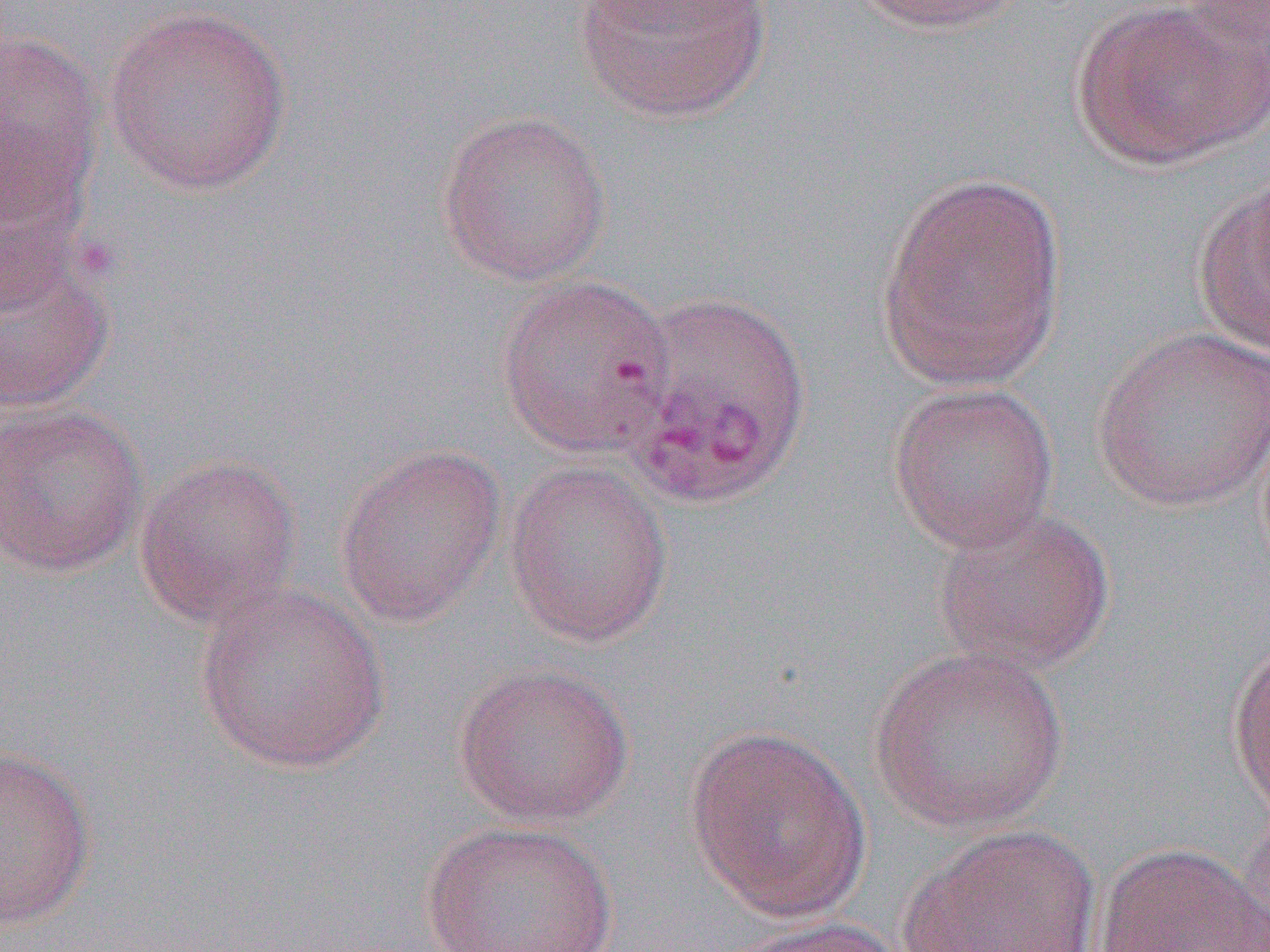
slide-level diagnosis = Plasmodium vivax
magnification = 1000x
field of view = single
modality = light microscopy
preparation = thin blood smear
image size = 1270×952 pixels
uninfected red blood cell locations (subset) = approximate bounding boxes as [x1, y1, x2, y2] in pixels: [581, 0, 771, 33], [845, 0, 1031, 35], [1070, 0, 1264, 169], [572, 1, 773, 124], [102, 6, 293, 196], [0, 30, 104, 215], [435, 109, 613, 286], [875, 168, 1069, 391], [1191, 170, 1270, 360], [0, 241, 116, 413], [495, 274, 676, 457], [1092, 326, 1270, 512], [887, 382, 1060, 553], [0, 400, 149, 579], [333, 443, 507, 627], [133, 453, 303, 629], [503, 460, 674, 647], [930, 505, 1116, 676], [193, 582, 391, 773], [1227, 638, 1270, 821], [869, 644, 1070, 833], [452, 662, 635, 827], [684, 724, 872, 922], [0, 744, 97, 932], [1237, 800, 1270, 952], [418, 819, 619, 952], [896, 824, 1102, 951], [1092, 842, 1269, 951], [724, 916, 908, 952]